Identify the parasite.
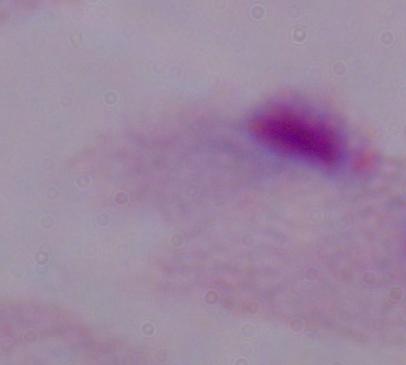

This is a trichomonad.

{
  "modality": "micrograph",
  "magnification": "1000x"
}